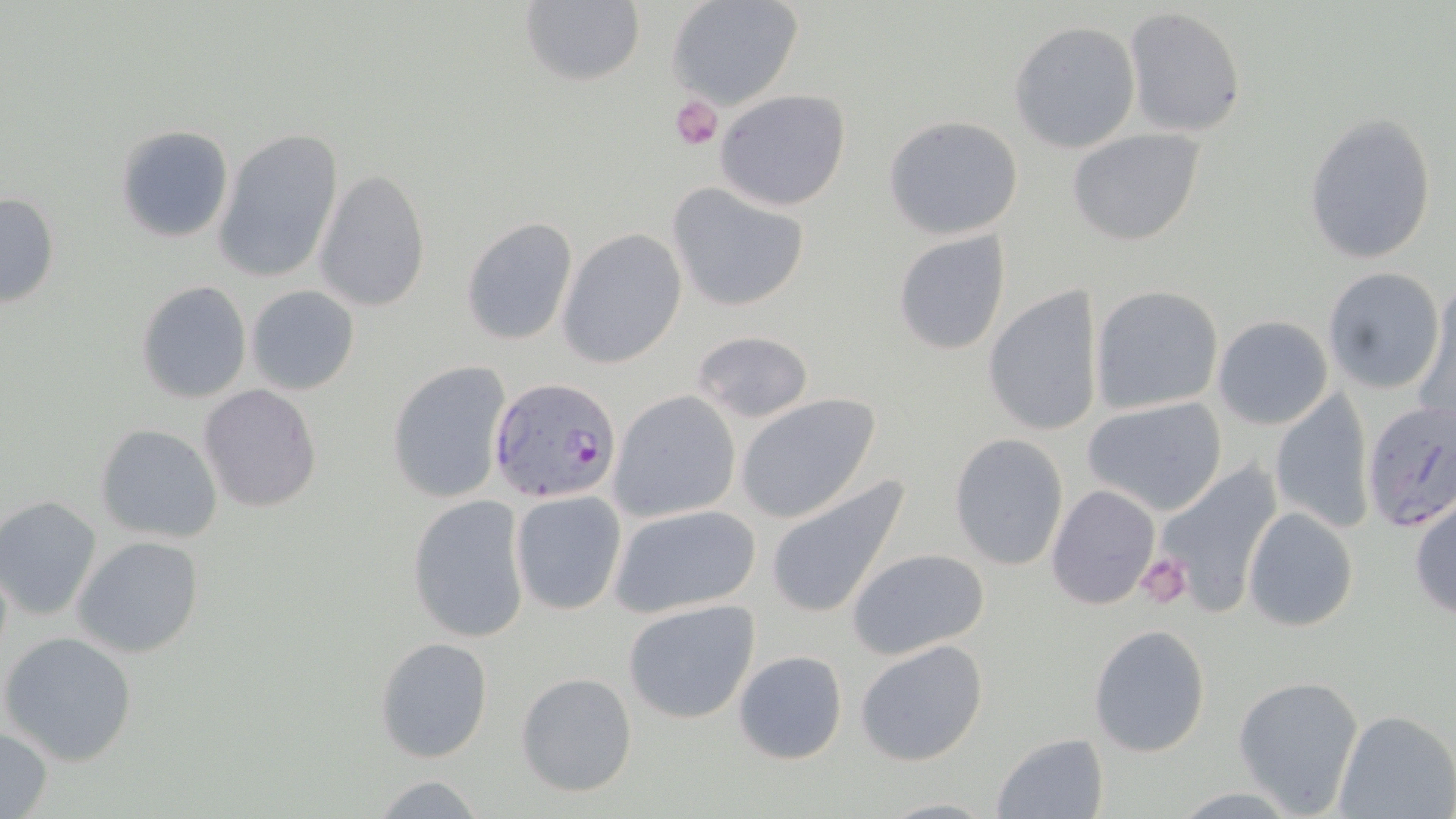

Approximate bounding boxes as (x1,y1)-(x2,y2) corner pairs in pixels. Uninfected red blood cell locations: (520,0)-(643,89), (665,0)-(803,111), (1124,8)-(1249,138), (1009,19)-(1141,154), (714,88)-(852,210), (1304,112)-(1437,264), (882,115)-(1026,240), (113,125)-(234,244), (1066,126)-(1207,246), (216,127)-(344,286), (314,168)-(431,313), (666,182)-(812,313), (1,191)-(60,309), (460,217)-(578,344), (557,228)-(687,368), (891,230)-(1012,356), (1322,266)-(1446,395), (137,280)-(251,403), (983,284)-(1105,438), (245,285)-(360,395), (1090,285)-(1224,414), (1416,286)-(1455,429), (1211,315)-(1334,429), (690,329)-(814,423), (386,359)-(512,505), (198,384)-(322,513), (1268,387)-(1375,534), (610,391)-(740,523), (734,393)-(880,523), (1084,396)-(1227,516), (95,423)-(224,543), (949,433)-(1071,571), (1153,461)-(1283,613), (765,473)-(912,621), (1047,484)-(1160,609), (509,491)-(627,614), (0,494)-(101,621), (406,494)-(531,643), (1408,494)-(1456,620), (607,503)-(764,618), (1242,506)-(1359,632), (72,536)-(204,659), (846,547)-(992,661), (621,598)-(763,724), (1087,624)-(1213,758), (1,631)-(137,766), (374,635)-(494,763), (854,637)-(989,766), (733,650)-(848,764), (515,671)-(638,797), (1232,674)-(1366,814), (1332,708)-(1455,819), (0,725)-(53,817), (991,733)-(1108,818), (367,772)-(491,818), (874,796)-(1003,817). Platelet locations: (669,94)-(722,150), (1136,555)-(1193,614). Plasmodium falciparum-infected red blood cell locations: (488,377)-(623,505), (1359,399)-(1456,534). Slide-level diagnosis: Plasmodium falciparum. May-Grünwald-Giemsa-stained preparation. Single field of view. Image is 1456×819 pixels. Thin blood film. Light microscopy. 1000x magnification.